Locate and identify every blood parasite.
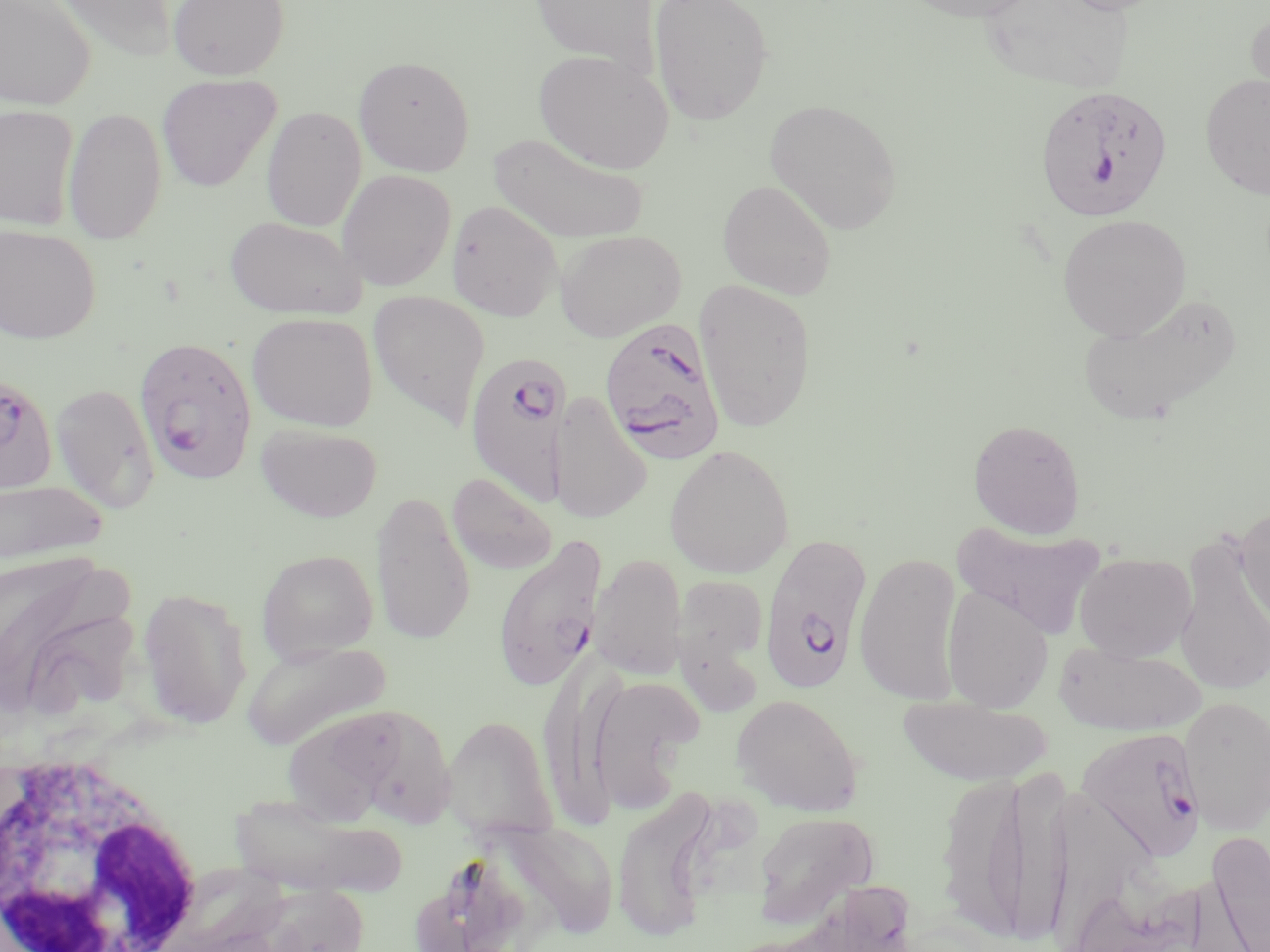

Approximate bounding boxes as (x1, y1, x2, y2) in pixels.
Plasmodium falciparum-infected red blood cells (subset): (1034, 84, 1174, 222), (598, 317, 727, 464), (134, 336, 258, 483), (464, 349, 572, 506), (0, 370, 58, 495), (759, 533, 872, 695), (492, 534, 607, 692).
No Plasmodium ovale, Plasmodium malariae, Plasmodium vivax, Babesia divergens, or Trypanosoma brucei observed.

Uninfected red blood cell locations (subset): (0, 0, 96, 110), (44, 0, 179, 63), (167, 0, 290, 80), (529, 0, 658, 70), (649, 0, 773, 124), (901, 0, 1042, 22), (978, 0, 1137, 95), (1053, 0, 1174, 15), (1245, 9, 1270, 117), (534, 50, 674, 174), (354, 55, 475, 176), (1200, 73, 1270, 199), (157, 74, 281, 192), (765, 98, 903, 235), (0, 105, 79, 230), (62, 106, 168, 245), (261, 106, 367, 232), (488, 132, 650, 244), (337, 169, 456, 291), (718, 179, 837, 300), (447, 199, 563, 321), (1057, 214, 1191, 342), (224, 215, 367, 320), (0, 224, 100, 344), (555, 229, 686, 342), (694, 279, 817, 432), (368, 289, 490, 427), (1078, 289, 1242, 425), (246, 312, 378, 431), (50, 382, 160, 512), (548, 393, 652, 527), (968, 419, 1086, 538), (256, 423, 383, 523), (664, 444, 794, 579), (447, 473, 558, 576), (1, 477, 109, 570), (370, 490, 476, 644), (1235, 505, 1270, 633), (953, 519, 1106, 638), (1173, 533, 1270, 699), (255, 548, 379, 662), (854, 552, 964, 704), (1075, 552, 1196, 662), (590, 553, 687, 681), (0, 564, 142, 720), (675, 575, 769, 666), (942, 586, 1054, 712), (136, 587, 253, 729), (242, 640, 389, 751), (1054, 641, 1206, 735), (585, 674, 704, 812), (731, 694, 863, 816), (896, 696, 1053, 786), (1178, 696, 1269, 836), (348, 705, 457, 837), (280, 707, 404, 826), (443, 714, 557, 840), (1004, 766, 1071, 947), (935, 770, 1035, 943), (611, 789, 718, 941), (229, 796, 405, 897), (752, 811, 878, 928), (504, 819, 618, 939), (1208, 833, 1270, 950), (1065, 880, 1202, 952), (248, 882, 372, 952). White blood cell locations: (2, 754, 206, 952). Slide-level diagnosis: Plasmodium falciparum. Thin blood smear. One field of a larger specimen. May-Grünwald-Giemsa-stained preparation. Optical microscopy. Captured at 1000x magnification. Image is 1270×952 pixels.